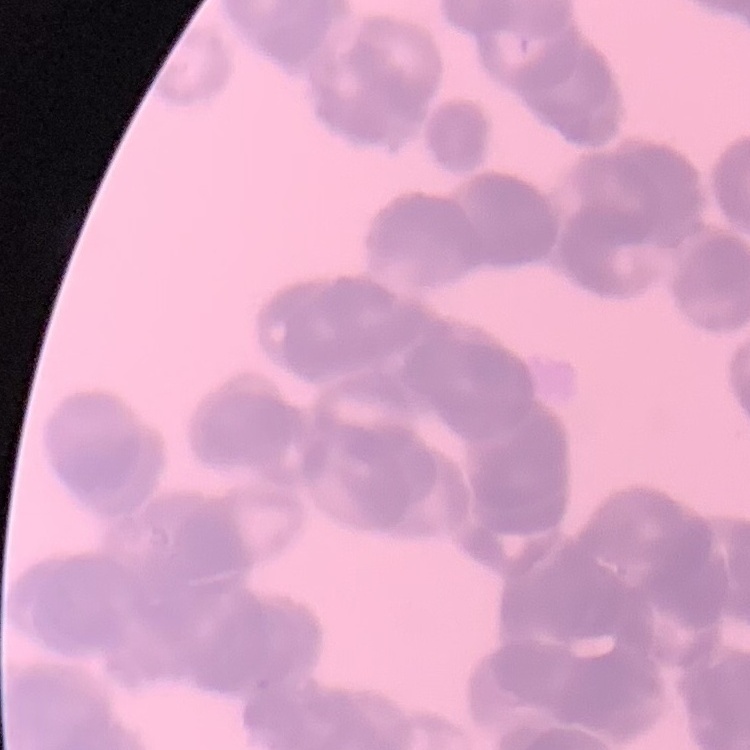
red blood cell morphology = rouleaux formation
preparation = thin peripheral smear
image type = square crop of a larger photomicrograph
stain = Field's or Giemsa